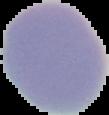
Summary:
  - Image size: 109×115 pixels
  - Preparation: thin blood film
  - Image type: cell region segmented out of the field of view; surrounding area masked to black
  - Result: no Plasmodium parasites seen